Assess this cell for malaria.
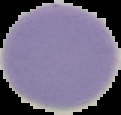
It is uninfected.

Summary:
  - Image size: 121×115 pixels
  - Image type: segmented cell region on a black background
  - Preparation: thin blood smear